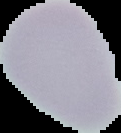

image size = 121×133 pixels
result = negative for malaria parasites
image type = cell region segmented out of the field of view; surrounding area masked to black
preparation = thin blood smear